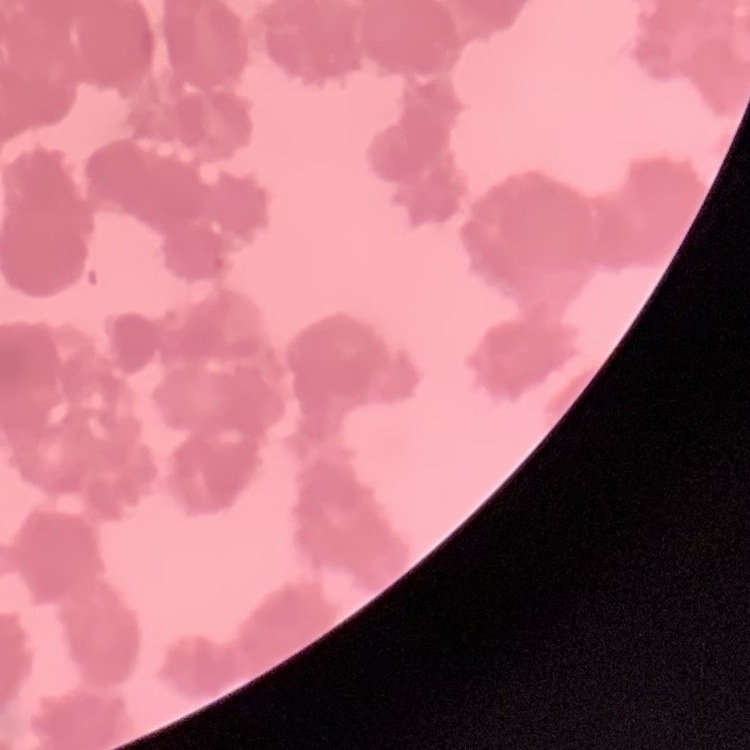 The red blood cells exhibit rouleaux formation. Square crop of a larger photomicrograph. Thin blood film. Stained with either Field's or Giemsa.